Name the cell type shown.
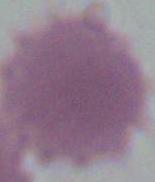
This is an erythrocyte.

Captured at 1000x magnification. Micrograph.